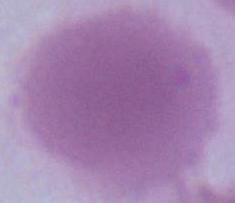

identification = red blood cell
modality = photomicrograph
magnification = 1000x